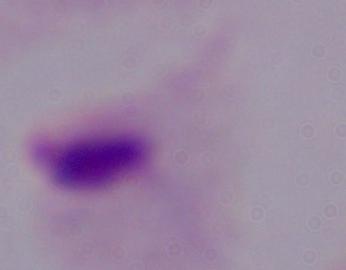

Summary:
  - Identification: trichomonad
  - Modality: micrograph
  - Magnification: 1000x